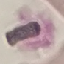
Malaria status: uninfected. Cell patch, automatically extracted from a larger field of view and resized to 64 × 64 pixels. Photographed with a smartphone camera at the microscope eyepiece. Thin blood smear. Giemsa stain.